Assess this cell for malaria.
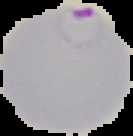
It is parasitized.

image size = 133×136 pixels
preparation = thin blood smear
image type = segmented cell region with the area outside set to black